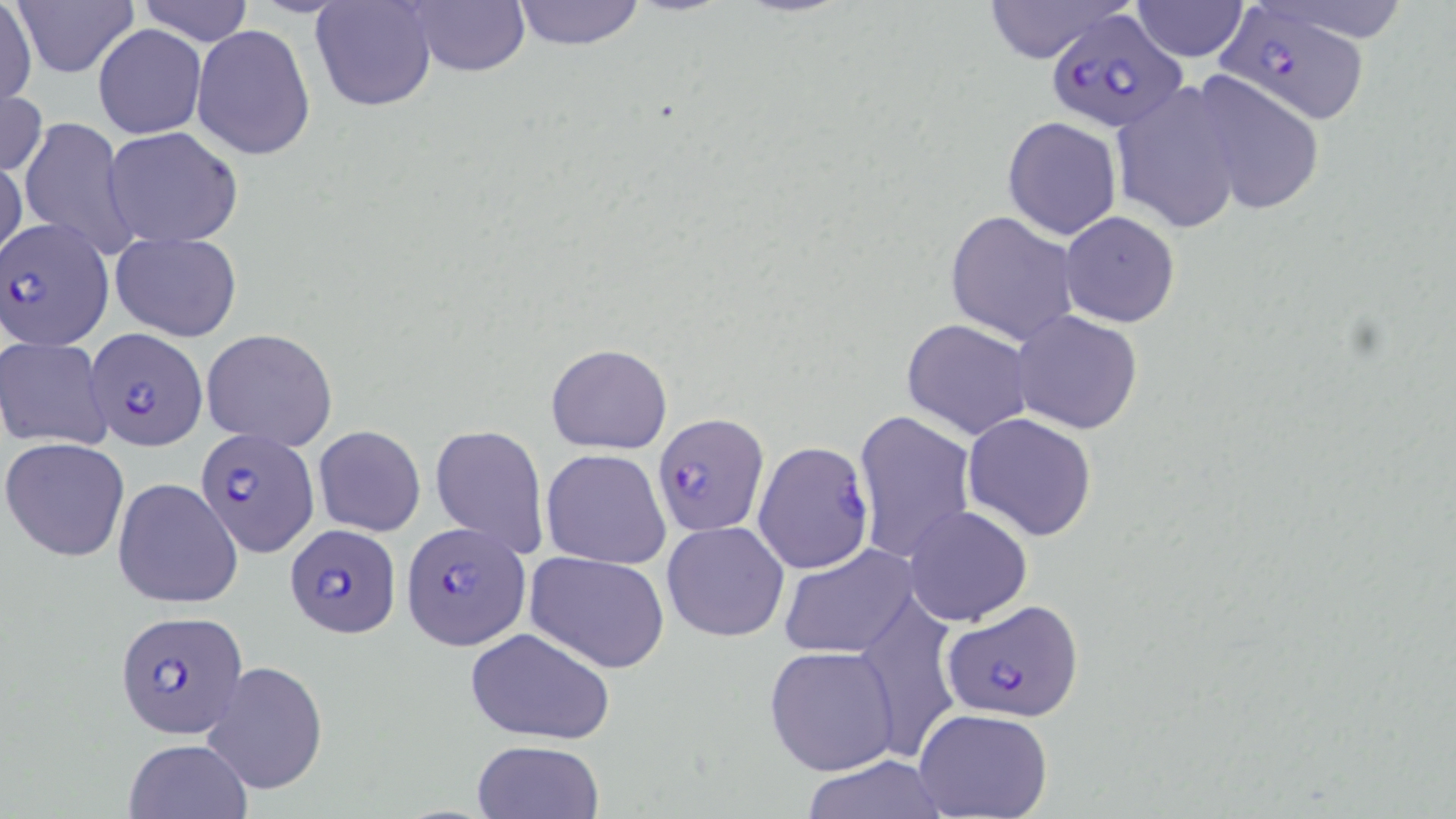

slide-level diagnosis = Plasmodium falciparum
uninfected red blood cell locations = approximate bounding boxes as (x1,y1)-(x2,y2) corner pairs in pixels: (0,0)-(37,111), (11,0)-(140,78), (136,0)-(255,46), (310,0)-(439,113), (401,0)-(532,76), (510,0)-(645,50), (977,0)-(1132,63), (1127,1)-(1253,61), (191,23)-(314,160), (94,25)-(206,139), (1188,72)-(1327,216), (1110,83)-(1247,235), (0,84)-(45,181), (20,116)-(135,260), (1002,116)-(1122,240), (104,125)-(244,247), (0,156)-(27,264), (944,210)-(1078,346), (1060,211)-(1180,326), (111,232)-(241,341), (1011,309)-(1143,434), (901,318)-(1034,440), (202,328)-(338,451), (0,338)-(113,450), (545,343)-(672,454), (853,408)-(977,565), (963,412)-(1097,541), (429,424)-(549,562), (314,425)-(426,536), (2,437)-(130,560), (541,448)-(671,567), (113,477)-(243,608), (903,504)-(1033,626), (662,520)-(790,642), (779,542)-(921,659), (525,551)-(670,673), (852,591)-(962,763), (463,627)-(616,744), (764,645)-(900,777), (200,660)-(328,796), (913,708)-(1055,819), (122,738)-(254,819), (471,739)-(603,819), (803,754)-(951,818)
Plasmodium falciparum-infected red blood cell locations = approximate bounding boxes as (x1,y1)-(x2,y2) corner pairs in pixels: (1220,4)-(1374,129), (1047,10)-(1185,131), (2,220)-(113,350), (87,328)-(207,450), (654,415)-(767,536), (195,427)-(318,558), (753,442)-(874,574), (286,523)-(400,637), (401,523)-(529,649), (944,598)-(1085,723), (115,607)-(246,737)
image size = 1456×819 pixels
magnification = 1000x
preparation = thin blood film
field of view = one of a larger specimen
stain = May-Grünwald-Giemsa
modality = light microscopy